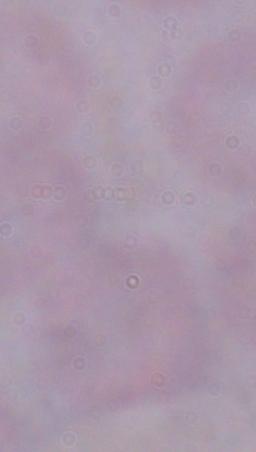
identification = trypanosome
modality = photomicrograph
magnification = 1000x